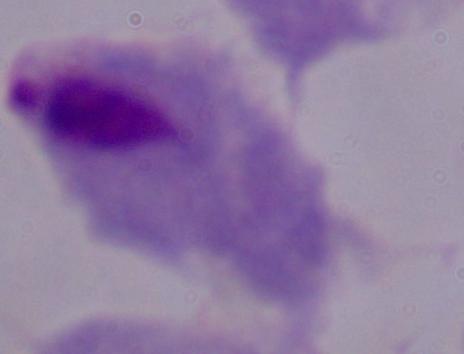 Micrograph. 1000x magnification. A trichomonad is shown.